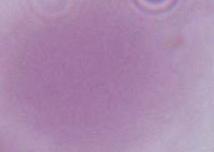

{
  "magnification": "1000x",
  "identification": "erythrocyte",
  "modality": "micrograph"
}